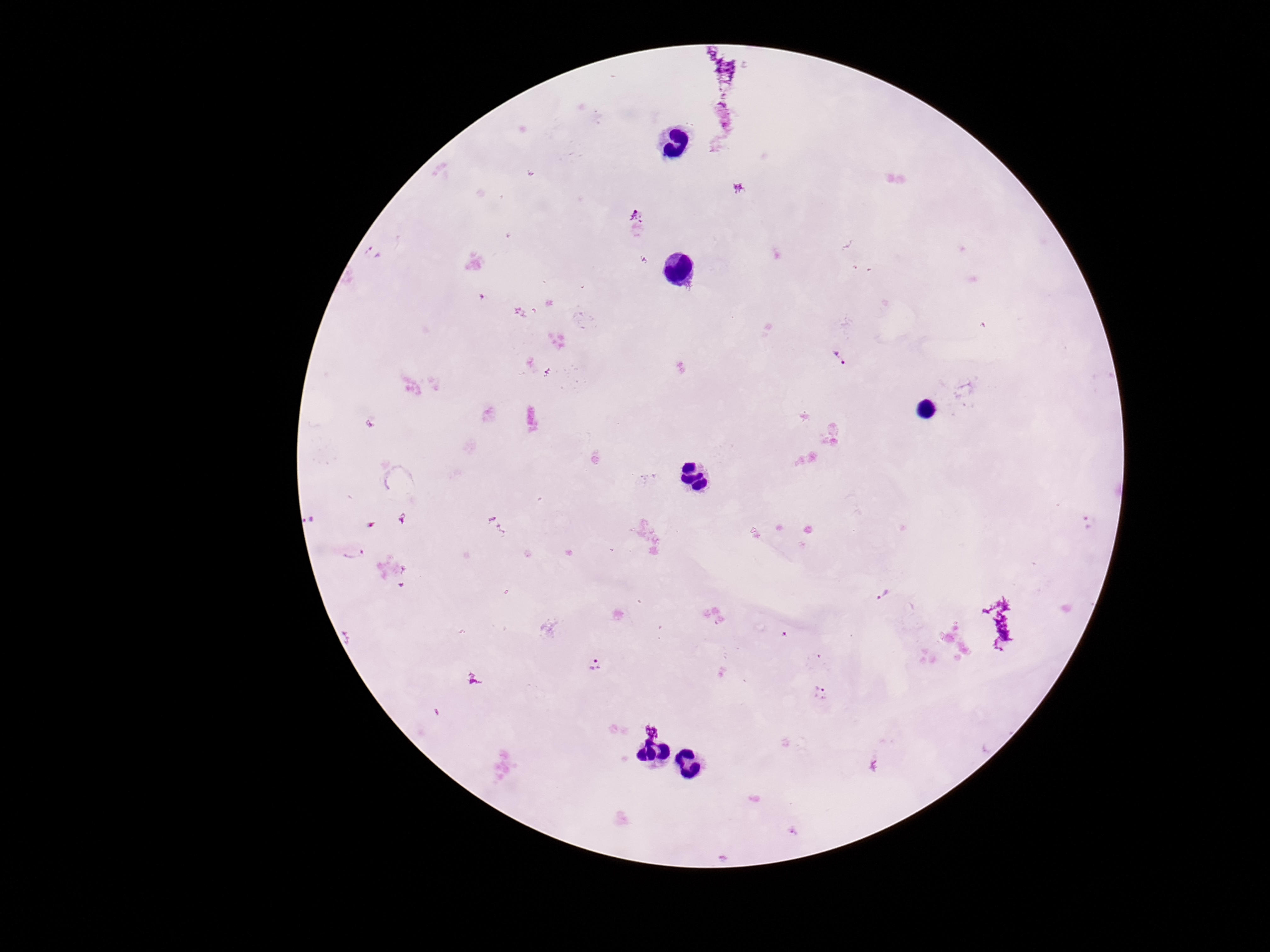

Approximate centers as (x, y) in pixels.
Summary:
  - Plasmodium parasite locations: (726, 72), (636, 217), (839, 358), (310, 520), (496, 523), (353, 551), (885, 595), (597, 666), (821, 694), (651, 730)
  - Field of view: single
  - Capture: smartphone camera through the microscope eyepiece
  - Patient malaria status: infected
  - Image size: 1270×952 pixels
  - Preparation: thick blood film
  - Magnification: 100x
  - Stain: Giemsa